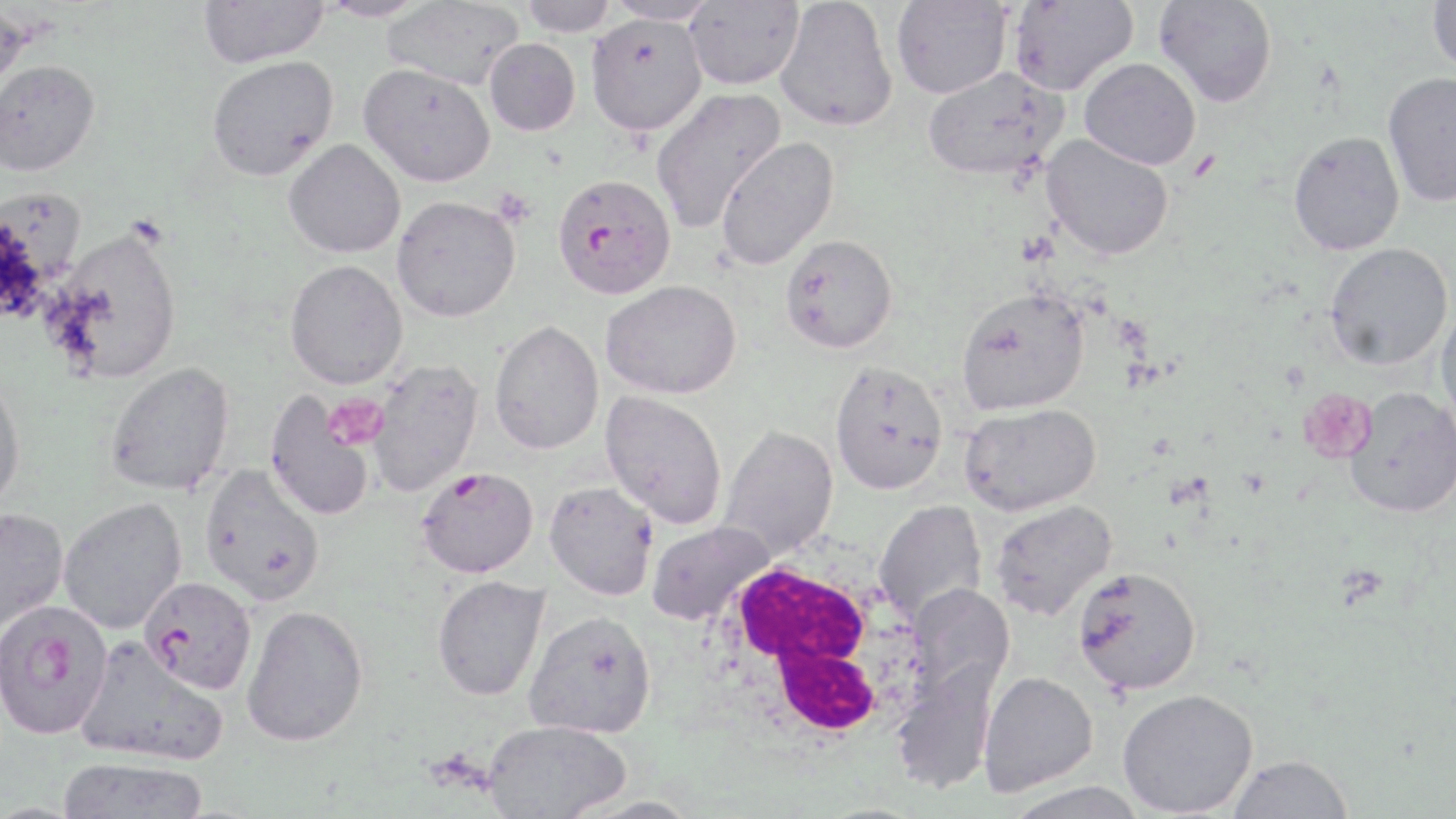
Approximate bounding boxes as named x1/y1/x2/y2 corners in pixels. Plasmodium falciparum-infected red blood cell locations: (x1=551, y1=171, x2=677, y2=298), (x1=416, y1=466, x2=539, y2=578), (x1=139, y1=576, x2=257, y2=694), (x1=0, y1=599, x2=114, y2=740). White blood cell locations: (x1=707, y1=555, x2=934, y2=751). Platelet locations: (x1=1298, y1=388, x2=1375, y2=463), (x1=321, y1=393, x2=388, y2=451). Uninfected red blood cell locations: (x1=198, y1=0, x2=330, y2=68), (x1=317, y1=0, x2=432, y2=22), (x1=518, y1=0, x2=619, y2=36), (x1=604, y1=0, x2=720, y2=25), (x1=775, y1=0, x2=898, y2=132), (x1=891, y1=0, x2=1012, y2=99), (x1=1008, y1=0, x2=1138, y2=95), (x1=1154, y1=0, x2=1277, y2=108), (x1=1427, y1=0, x2=1456, y2=76), (x1=382, y1=1, x2=524, y2=90), (x1=684, y1=1, x2=804, y2=90), (x1=0, y1=2, x2=33, y2=112), (x1=585, y1=13, x2=707, y2=135), (x1=484, y1=38, x2=580, y2=136), (x1=206, y1=55, x2=339, y2=180), (x1=1079, y1=57, x2=1201, y2=169), (x1=0, y1=60, x2=100, y2=179), (x1=358, y1=63, x2=496, y2=187), (x1=923, y1=66, x2=1068, y2=180), (x1=1383, y1=71, x2=1456, y2=208), (x1=650, y1=87, x2=786, y2=232), (x1=1288, y1=130, x2=1405, y2=255), (x1=1040, y1=134, x2=1174, y2=260), (x1=715, y1=136, x2=840, y2=270), (x1=283, y1=139, x2=406, y2=258), (x1=391, y1=195, x2=521, y2=322), (x1=54, y1=227, x2=183, y2=383), (x1=779, y1=233, x2=898, y2=354), (x1=1325, y1=242, x2=1453, y2=370), (x1=284, y1=260, x2=408, y2=389), (x1=601, y1=279, x2=741, y2=399), (x1=955, y1=285, x2=1089, y2=414), (x1=1435, y1=304, x2=1456, y2=430), (x1=489, y1=319, x2=604, y2=455), (x1=368, y1=359, x2=483, y2=496), (x1=830, y1=360, x2=949, y2=495), (x1=106, y1=361, x2=235, y2=496), (x1=0, y1=372, x2=26, y2=513), (x1=1345, y1=388, x2=1456, y2=517), (x1=601, y1=390, x2=727, y2=528), (x1=264, y1=391, x2=374, y2=521), (x1=960, y1=402, x2=1100, y2=516), (x1=719, y1=426, x2=839, y2=559), (x1=199, y1=464, x2=325, y2=606), (x1=545, y1=481, x2=658, y2=600), (x1=58, y1=497, x2=186, y2=634), (x1=873, y1=500, x2=987, y2=624), (x1=990, y1=500, x2=1117, y2=620), (x1=0, y1=508, x2=69, y2=636), (x1=647, y1=521, x2=776, y2=626), (x1=1072, y1=566, x2=1202, y2=694), (x1=431, y1=575, x2=550, y2=701), (x1=906, y1=584, x2=1013, y2=704), (x1=241, y1=604, x2=368, y2=747), (x1=523, y1=610, x2=657, y2=738), (x1=75, y1=636, x2=228, y2=767), (x1=892, y1=661, x2=1000, y2=795), (x1=978, y1=671, x2=1098, y2=797), (x1=1118, y1=688, x2=1259, y2=817), (x1=483, y1=718, x2=631, y2=818), (x1=1227, y1=753, x2=1354, y2=818), (x1=56, y1=756, x2=210, y2=819), (x1=1003, y1=780, x2=1148, y2=819). Slide-level diagnosis: Plasmodium falciparum. Optical microscopy. Single field of view. May-Grünwald-Giemsa stain. Captured at 1000x magnification. Image is 1456×819 pixels. Thin blood smear.